Assess the morphology of the erythrocytes.
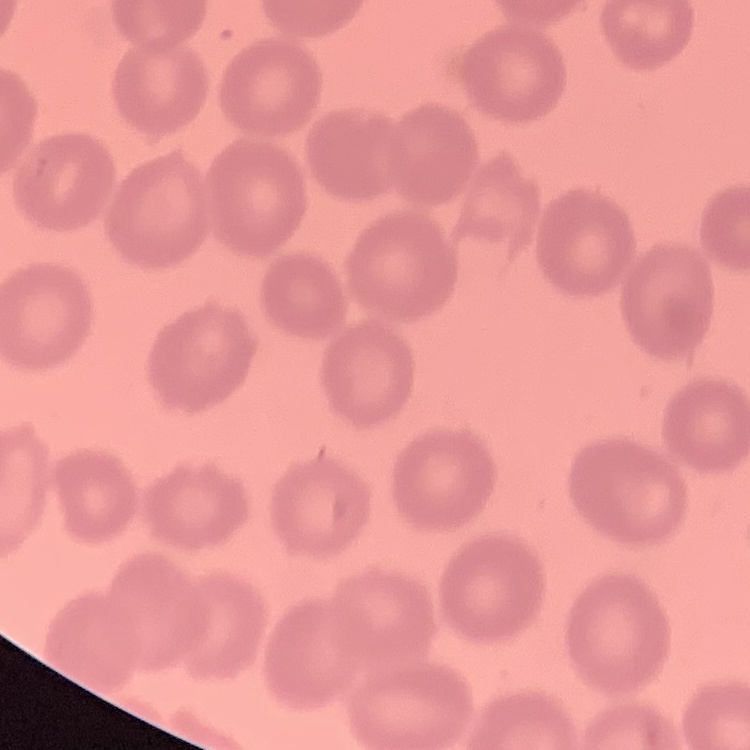

No rouleaux formation.

Thin peripheral smear. One tile cut from a larger photomicrograph. Field's or Giemsa stain.